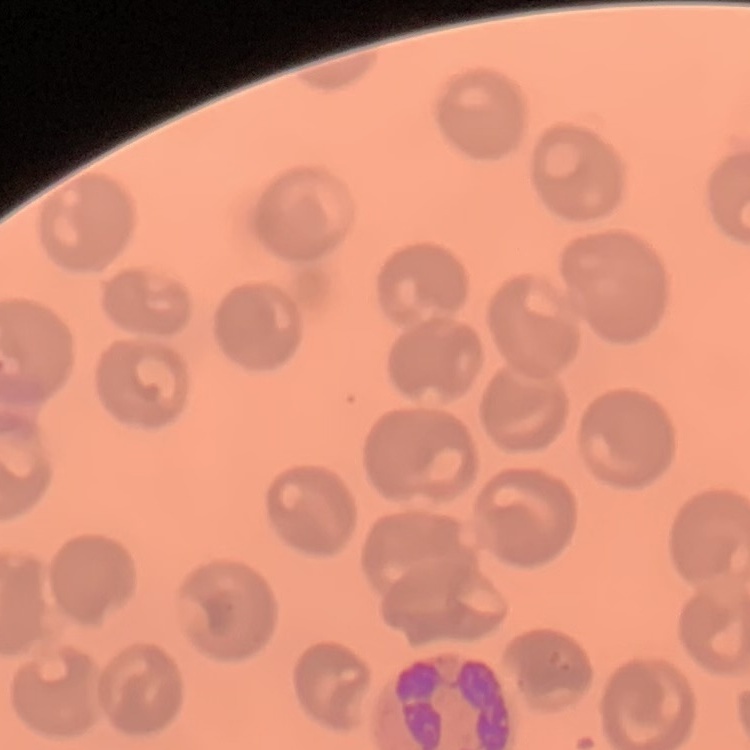

Summary:
  - Red blood cell morphology: no rouleaux formation
  - Image type: square crop of a larger photomicrograph
  - Preparation: thin peripheral smear
  - Stain: Field's or Giemsa